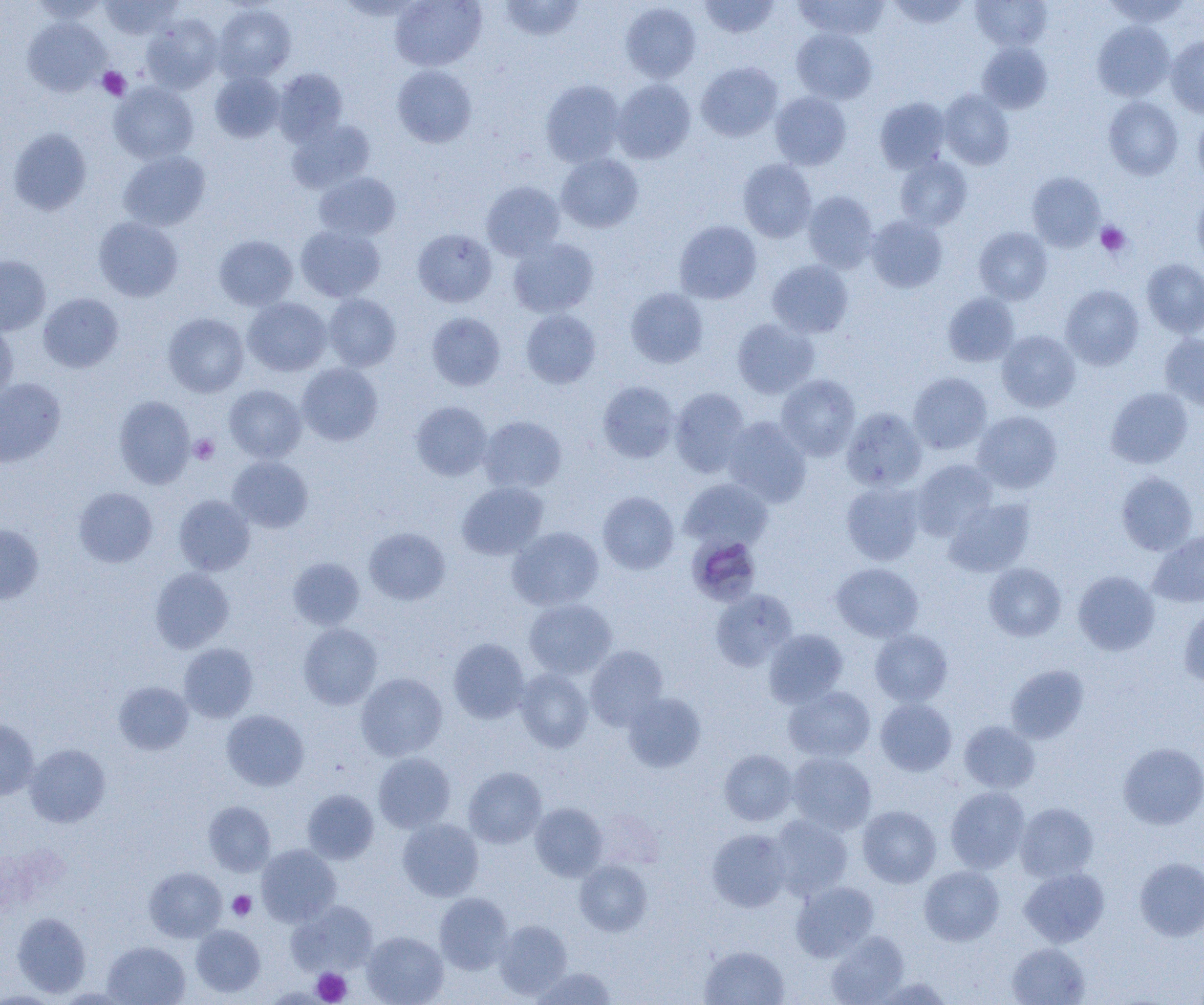 Approximate bounding boxes as (x1,y1)-(x2,y2) corner pairs in pixels. Platelet locations: (97,67)-(130,100), (1095,221)-(1132,258), (189,434)-(219,465), (228,891)-(256,920), (312,968)-(351,1004). Uninfected red blood cell locations: (28,0)-(109,23), (99,0)-(182,40), (390,0)-(486,71), (500,0)-(584,41), (699,0)-(780,38), (793,0)-(889,39), (887,0)-(970,29), (971,0)-(1052,51), (1102,0)-(1192,28), (621,3)-(702,83), (213,4)-(296,83), (141,15)-(223,94), (23,17)-(109,96), (1092,21)-(1175,101), (791,28)-(877,104), (1166,36)-(1204,118), (977,42)-(1052,113), (696,62)-(783,142), (392,65)-(476,147), (274,68)-(348,145), (210,71)-(284,142), (612,79)-(696,163), (540,80)-(625,167), (109,81)-(199,164), (939,89)-(1014,170), (770,91)-(851,170), (874,96)-(951,174), (1103,96)-(1184,180), (1193,112)-(1204,187), (287,119)-(374,193), (8,128)-(92,216), (118,151)-(210,231), (556,153)-(643,233), (895,155)-(972,231), (738,159)-(816,242), (314,172)-(400,240), (1027,172)-(1105,251), (481,181)-(565,260), (803,190)-(879,273), (1192,190)-(1204,268), (865,214)-(948,293), (93,217)-(183,302), (674,220)-(762,304), (296,225)-(385,302), (974,226)-(1052,304), (412,228)-(497,307), (214,235)-(298,311), (508,237)-(598,318), (0,255)-(51,336), (1141,258)-(1204,338), (767,259)-(853,337), (1061,284)-(1144,370), (625,287)-(708,368), (38,293)-(124,372), (943,293)-(1020,366), (323,294)-(401,371), (243,297)-(331,376), (521,309)-(601,388), (427,312)-(506,391), (163,313)-(249,397), (732,318)-(819,398), (0,321)-(18,402), (996,330)-(1080,412), (1160,333)-(1204,411), (297,363)-(383,445), (908,373)-(991,454), (776,374)-(861,460), (0,377)-(66,467), (597,380)-(680,463), (224,384)-(306,463), (1106,386)-(1193,468), (670,388)-(750,476), (114,396)-(195,488), (410,401)-(492,480), (841,407)-(927,491), (973,411)-(1062,493), (479,415)-(567,493), (723,417)-(811,506), (227,456)-(313,533), (911,459)-(998,540), (1116,472)-(1198,555), (680,478)-(772,551), (457,481)-(548,560), (841,482)-(924,565), (73,487)-(158,567), (597,491)-(679,574), (174,495)-(255,575), (944,497)-(1035,577), (0,524)-(43,604), (508,526)-(604,610), (364,527)-(450,605), (1147,529)-(1204,608), (288,557)-(364,630), (983,562)-(1066,641), (831,563)-(923,641), (150,567)-(234,653), (1073,570)-(1160,655), (710,589)-(797,671), (524,599)-(617,679), (1178,603)-(1204,688), (298,623)-(382,709), (764,629)-(848,707), (870,629)-(953,707), (448,638)-(530,723), (179,643)-(258,722), (585,645)-(668,730), (1006,664)-(1090,743), (515,668)-(593,752), (356,673)-(447,761), (113,681)-(194,755), (783,686)-(875,762), (622,691)-(706,773), (875,698)-(957,776), (222,710)-(309,791), (0,718)-(39,800), (959,720)-(1040,793), (1118,742)-(1204,829), (25,743)-(110,827), (719,750)-(798,825), (373,752)-(455,832), (786,752)-(876,834), (463,767)-(546,848), (945,786)-(1030,874), (302,789)-(379,864), (203,801)-(275,876), (1015,802)-(1098,882), (530,803)-(608,881), (857,805)-(941,888), (769,814)-(853,900), (398,819)-(483,901), (707,829)-(791,912), (257,844)-(340,926), (1134,857)-(1204,941), (575,859)-(652,936), (919,865)-(1004,945), (144,866)-(226,941), (1019,866)-(1109,947), (791,881)-(879,961), (435,892)-(513,974), (291,900)-(378,975), (12,911)-(91,997), (494,919)-(572,999), (190,924)-(265,997), (362,931)-(448,1005), (826,931)-(909,1005), (102,941)-(190,1005), (1007,942)-(1090,1005), (699,945)-(790,1005), (531,966)-(618,1005), (869,976)-(956,1005). Plasmodium malariae-infected red blood cell locations: (685,540)-(764,601). Slide-level diagnosis: Plasmodium malariae. Thin blood film. Image is 1204×1005 pixels. Single field of view. Captured at 1000x magnification. Optical microscopy.